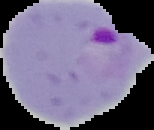

{
  "image_size": "154×130 pixels",
  "malaria_status": "parasitized",
  "preparation": "thin blood smear",
  "image_type": "cell region segmented out of the field of view; surrounding area masked to black"
}